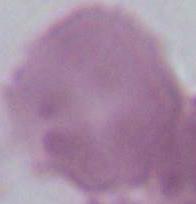
Summary:
  - Modality: photomicrograph
  - Identification: red blood cell
  - Magnification: 1000x